Report the malaria status of this cell.
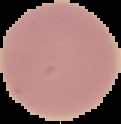

Uninfected.

image size = 121×124 pixels
image type = cell region segmented out of the field of view; surrounding area masked to black
preparation = thin blood film